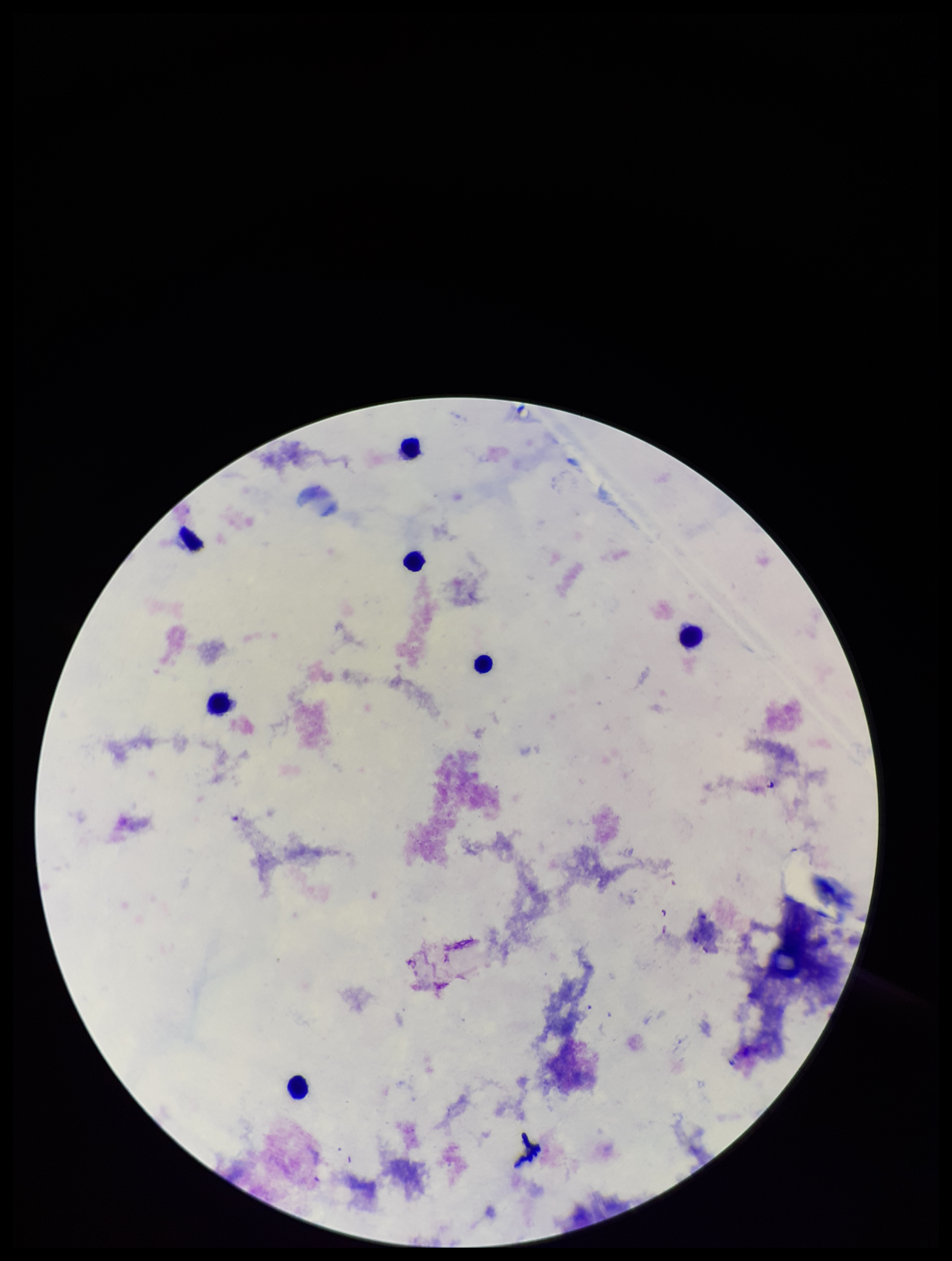

Plasmodium parasites = none detected
preparation = thick
image size = 952×1261 pixels
patient malaria status = negative
field of view = one from this slide
stain = Giemsa
parasite count = 0
capture = smartphone photograph through the microscope eyepiece
leukocyte count = 7